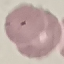
Summary:
  - Result: malaria parasites identified
  - Capture: smartphone through the microscope eyepiece
  - Preparation: thin blood film
  - Image type: automatically extracted cell patch, resized to 64 × 64 pixels
  - Stain: Giemsa